Assess this cell for malaria.
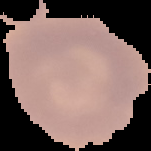
It is uninfected.

preparation = thin blood film
image size = 151×151 pixels
image type = cell region segmented out of the field of view; surrounding area masked to black